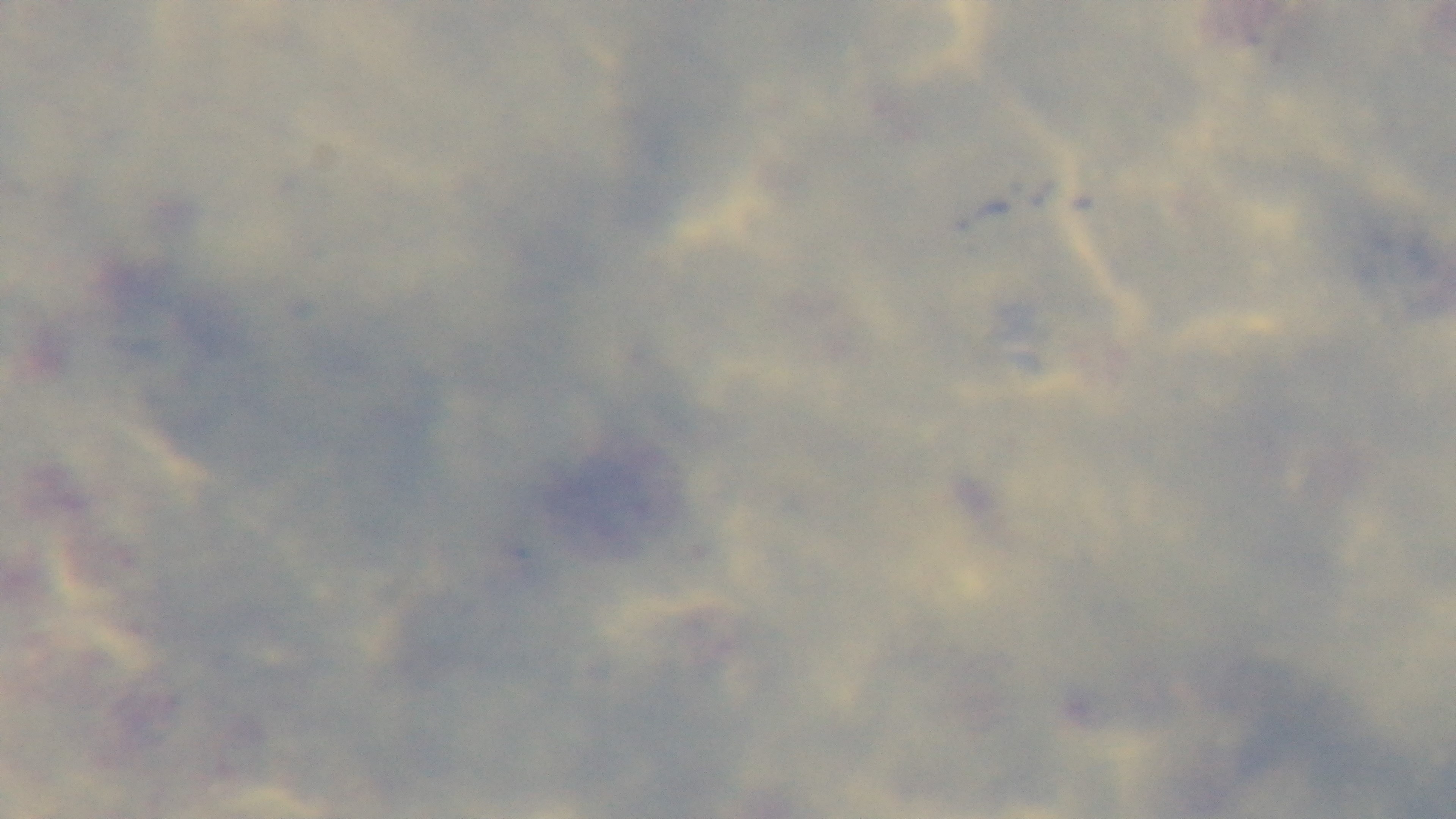
{
  "malaria_status": "uninfected",
  "stain": "Giemsa",
  "preparation": "thick smear",
  "objective": "100x oil immersion",
  "field_of_view": "single",
  "capture": "mounted 4K digital camera",
  "modality": "light microscopy"
}